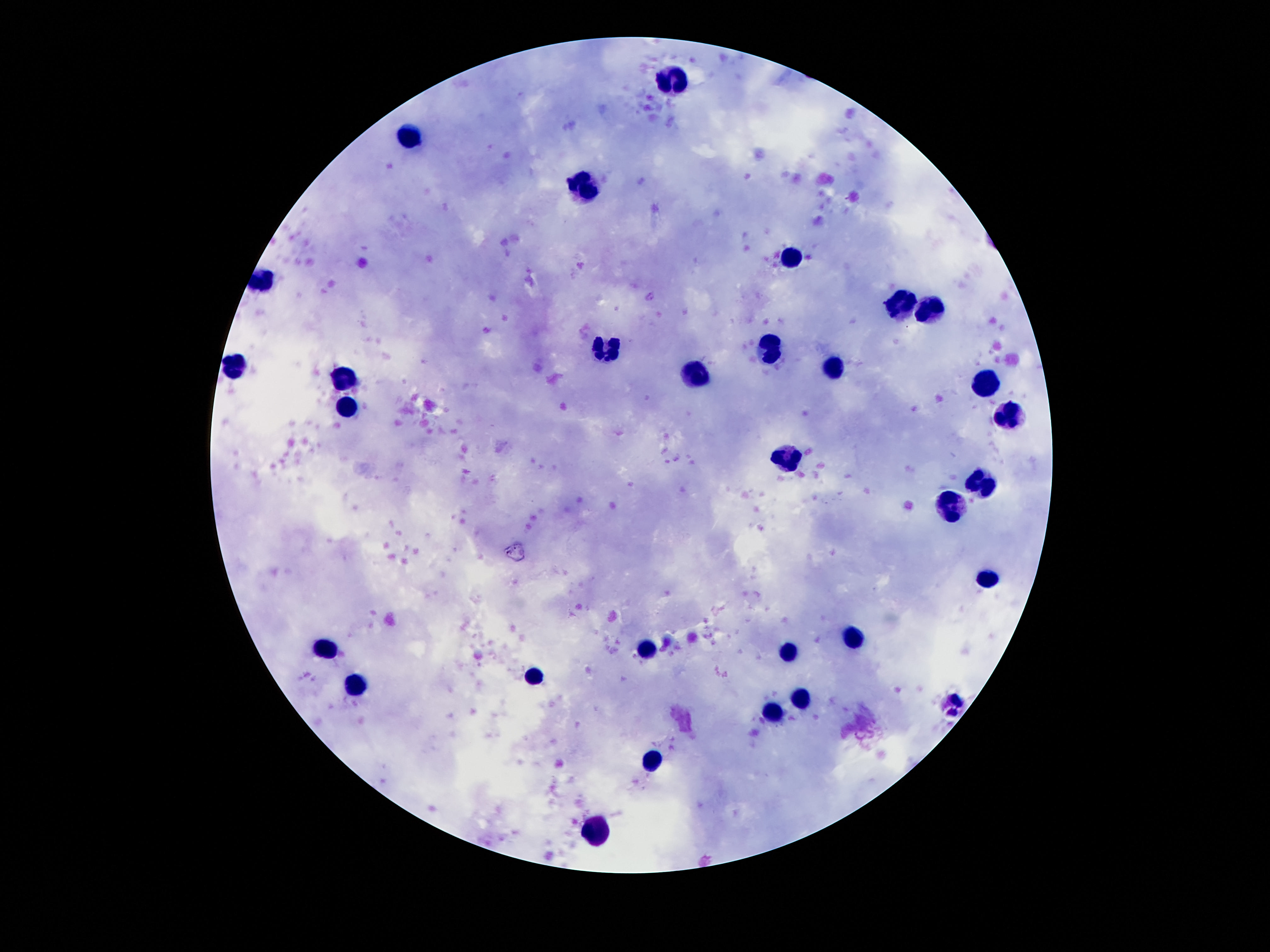

Approximate centers as (x, y) in pixels.
Summary:
  - Leukocyte locations: (672, 81), (408, 137), (586, 186), (792, 256), (261, 280), (903, 303), (928, 312), (773, 351), (605, 352), (234, 370), (836, 370), (695, 375), (345, 379), (985, 382), (345, 409), (1008, 417), (784, 458), (981, 486), (952, 501), (989, 580), (851, 640), (328, 647), (645, 649), (786, 652), (534, 676), (355, 686), (800, 699), (773, 713), (655, 760), (597, 831)
  - Preparation: thick blood film
  - Magnification: 100x
  - Field of view: one from this slide
  - Capture: smartphone camera through the microscope eyepiece
  - Patient malaria status: not infected
  - Stain: Giemsa
  - Image size: 1270×952 pixels